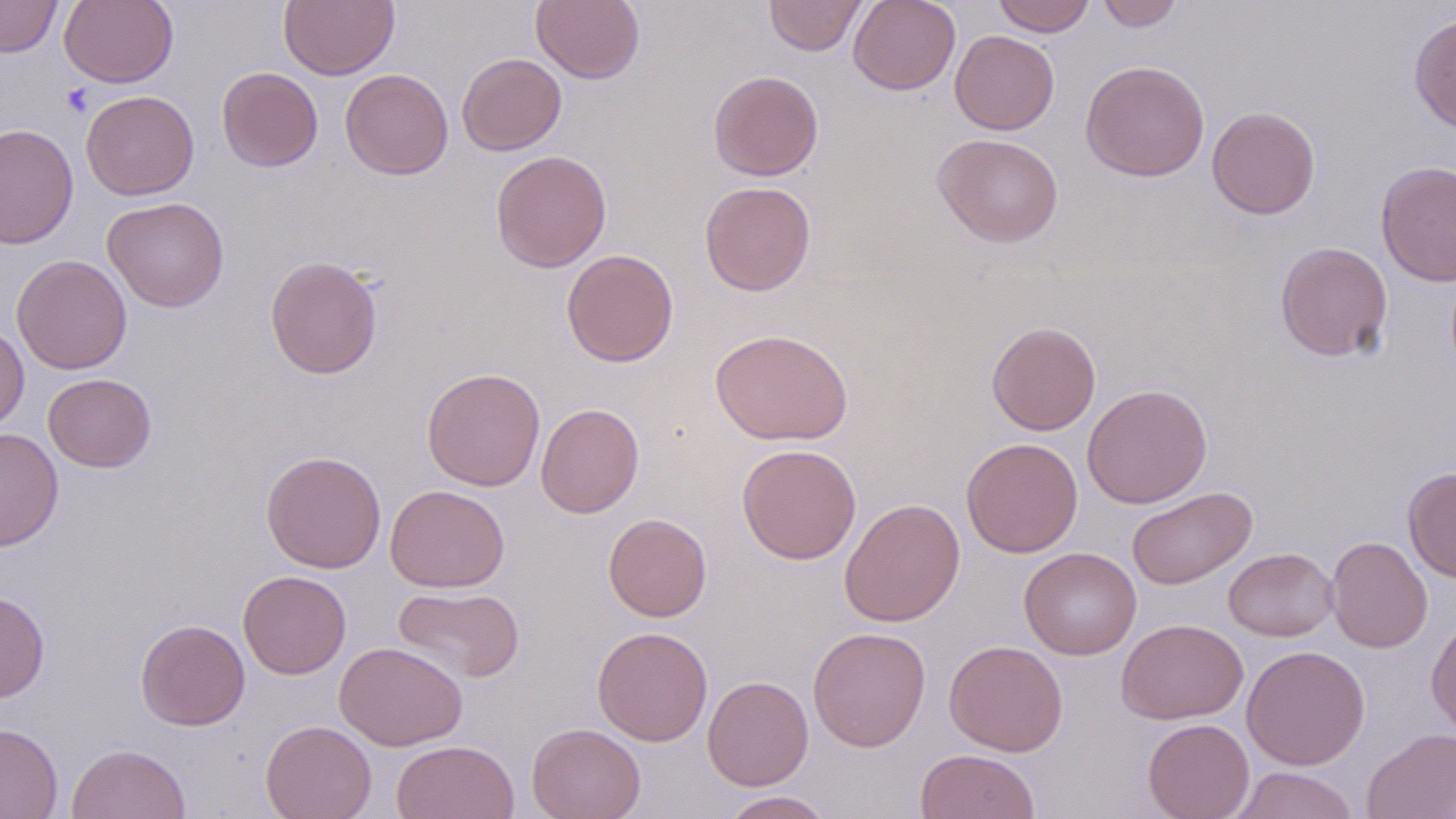

slide-level diagnosis = negative for blood parasites
image size = 1456×819 pixels
field of view = single
stain = May-Grünwald-Giemsa
uninfected red blood cell locations = approximate bounding boxes as (x1, y1, x2, y2) in pixels: (0, 0, 62, 58), (59, 0, 179, 88), (279, 0, 399, 80), (531, 0, 645, 84), (765, 0, 867, 56), (848, 0, 961, 95), (992, 0, 1096, 36), (1096, 0, 1184, 31), (1408, 13, 1456, 134), (950, 30, 1059, 135), (457, 52, 567, 155), (1081, 60, 1210, 181), (216, 66, 323, 172), (340, 68, 453, 180), (708, 70, 824, 181), (81, 90, 199, 200), (1206, 106, 1321, 219), (0, 123, 79, 249), (933, 133, 1064, 247), (490, 150, 612, 272), (1375, 159, 1456, 287), (699, 180, 816, 296), (102, 197, 230, 312), (1274, 241, 1394, 362), (561, 249, 679, 367), (11, 254, 133, 375), (265, 255, 383, 380), (986, 321, 1101, 435), (0, 323, 29, 432), (710, 327, 853, 446), (421, 367, 545, 491), (43, 373, 156, 472), (1082, 383, 1213, 509), (536, 403, 644, 518), (0, 427, 64, 552), (961, 438, 1083, 558), (736, 443, 861, 564), (260, 450, 387, 573), (1403, 466, 1456, 583), (385, 485, 509, 592), (1126, 486, 1258, 590), (839, 498, 966, 627), (604, 513, 712, 621), (1326, 536, 1432, 653), (1019, 547, 1141, 660), (1224, 547, 1338, 641), (238, 570, 351, 679), (393, 585, 525, 683), (0, 589, 50, 703), (1426, 614, 1456, 739), (135, 618, 250, 730), (1116, 618, 1248, 725), (591, 626, 712, 746), (808, 627, 931, 751), (944, 640, 1068, 757), (335, 642, 467, 750), (1241, 645, 1370, 770), (703, 675, 813, 790), (1143, 718, 1254, 819), (260, 720, 376, 819), (527, 722, 646, 819), (0, 723, 63, 818), (1362, 727, 1456, 819), (391, 740, 519, 819), (66, 743, 191, 819), (915, 749, 1041, 819), (1228, 766, 1360, 818), (719, 790, 835, 818)
modality = light microscopy
platelet locations = approximate bounding boxes as (x1, y1, x2, y2) in pixels: (61, 83, 94, 117)
preparation = thin blood smear
magnification = 1000x